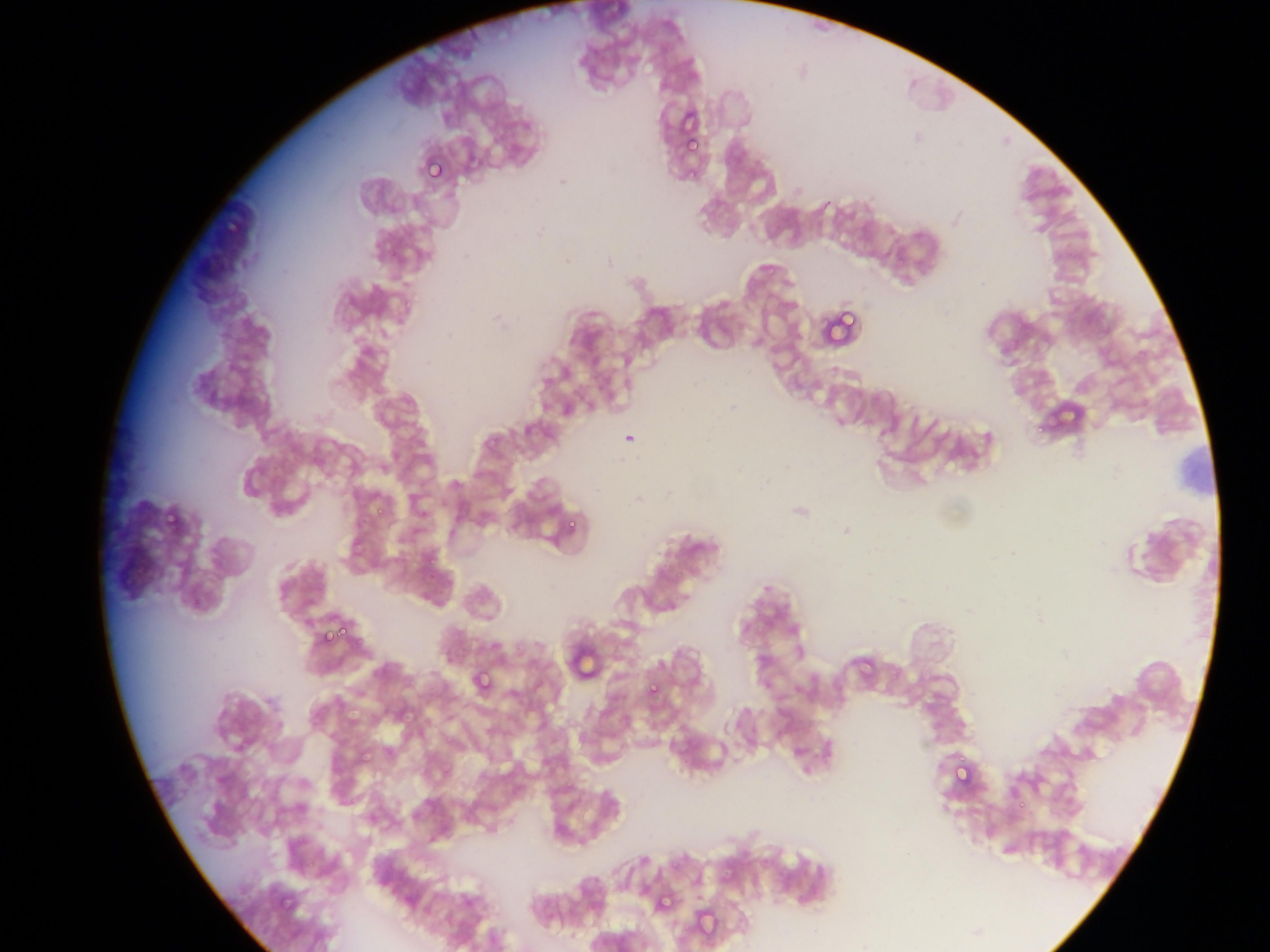 Approximate bounding boxes as [left, top, right, bottom] in pixels. Plasmodium parasite locations: [673, 112, 713, 164], [681, 133, 706, 159], [421, 154, 451, 187], [218, 208, 242, 240], [816, 304, 863, 349], [372, 493, 396, 519], [161, 510, 179, 525], [565, 520, 583, 537], [417, 548, 437, 572], [312, 615, 344, 647], [476, 670, 493, 691], [644, 680, 664, 703], [951, 749, 982, 792], [652, 884, 678, 911], [692, 900, 721, 939]. Mobile-phone photograph taken through the microscope. Image is 1270×952 pixels. Collected in Ghana. Single field of view. Thin blood film.